Describe the morphology of the red blood cells.
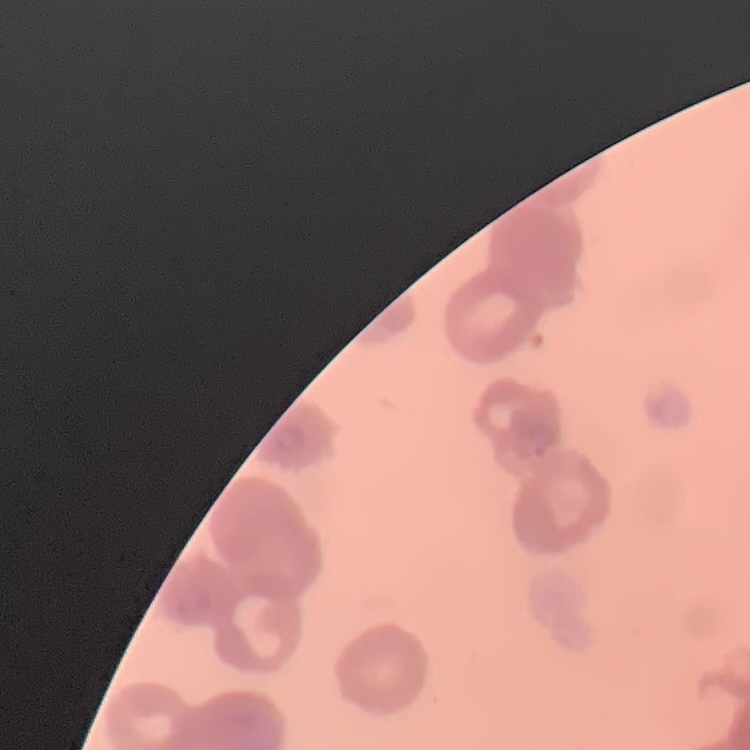
Rouleaux formation.

Thin peripheral smear. Square crop of a larger photomicrograph. Field's or Giemsa stain.